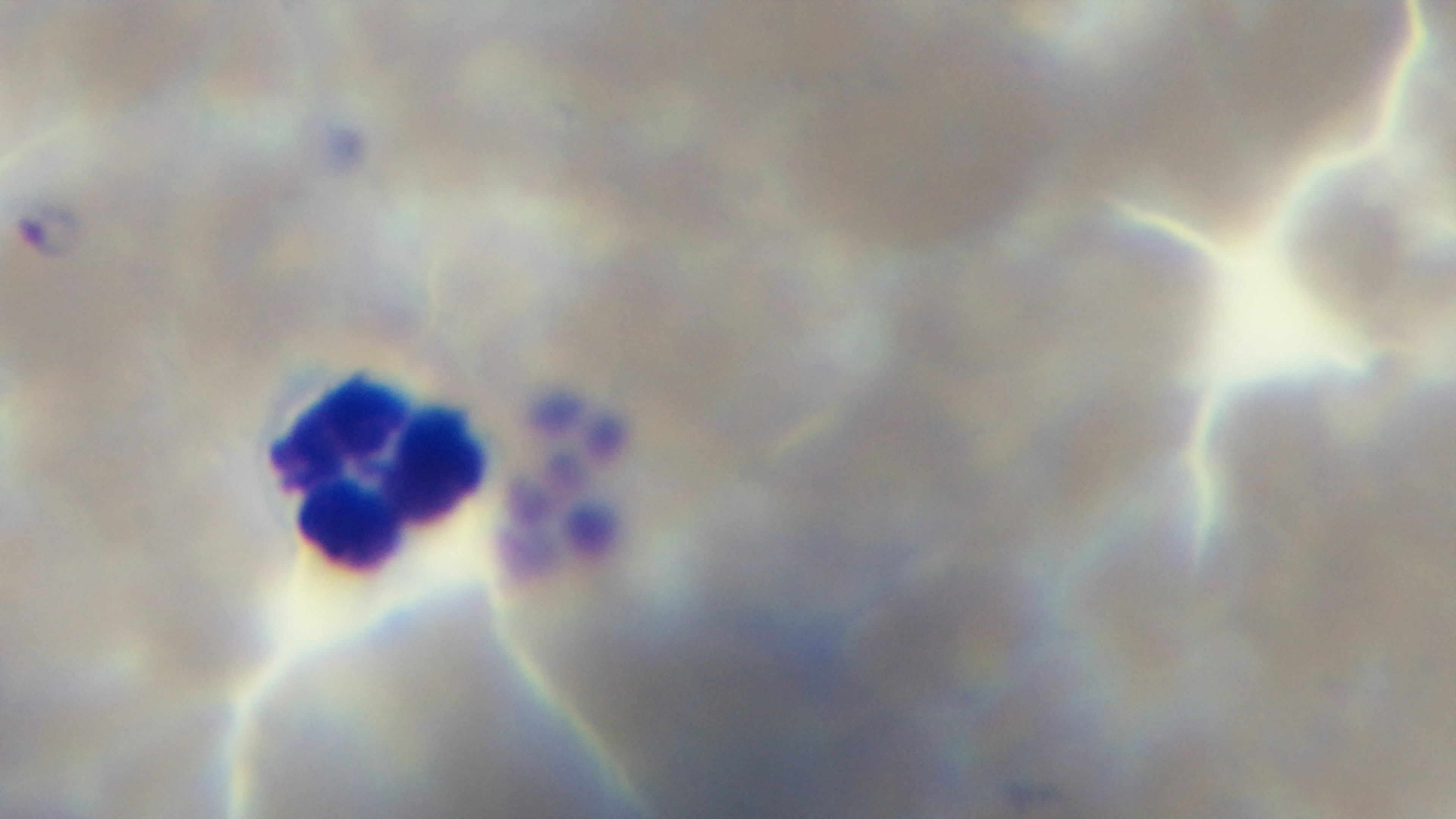

Summary:
  - Malaria status: infected
  - Preparation: thin
  - Stain: Giemsa
  - Capture: mounted 4K digital camera
  - Field of view: single
  - Objective: 100x oil immersion
  - Modality: light microscopy